Name the parasite shown.
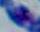

Toxoplasma gondii.

magnification: 1000x
modality: micrograph